Locate every blood parasite and identify its species.
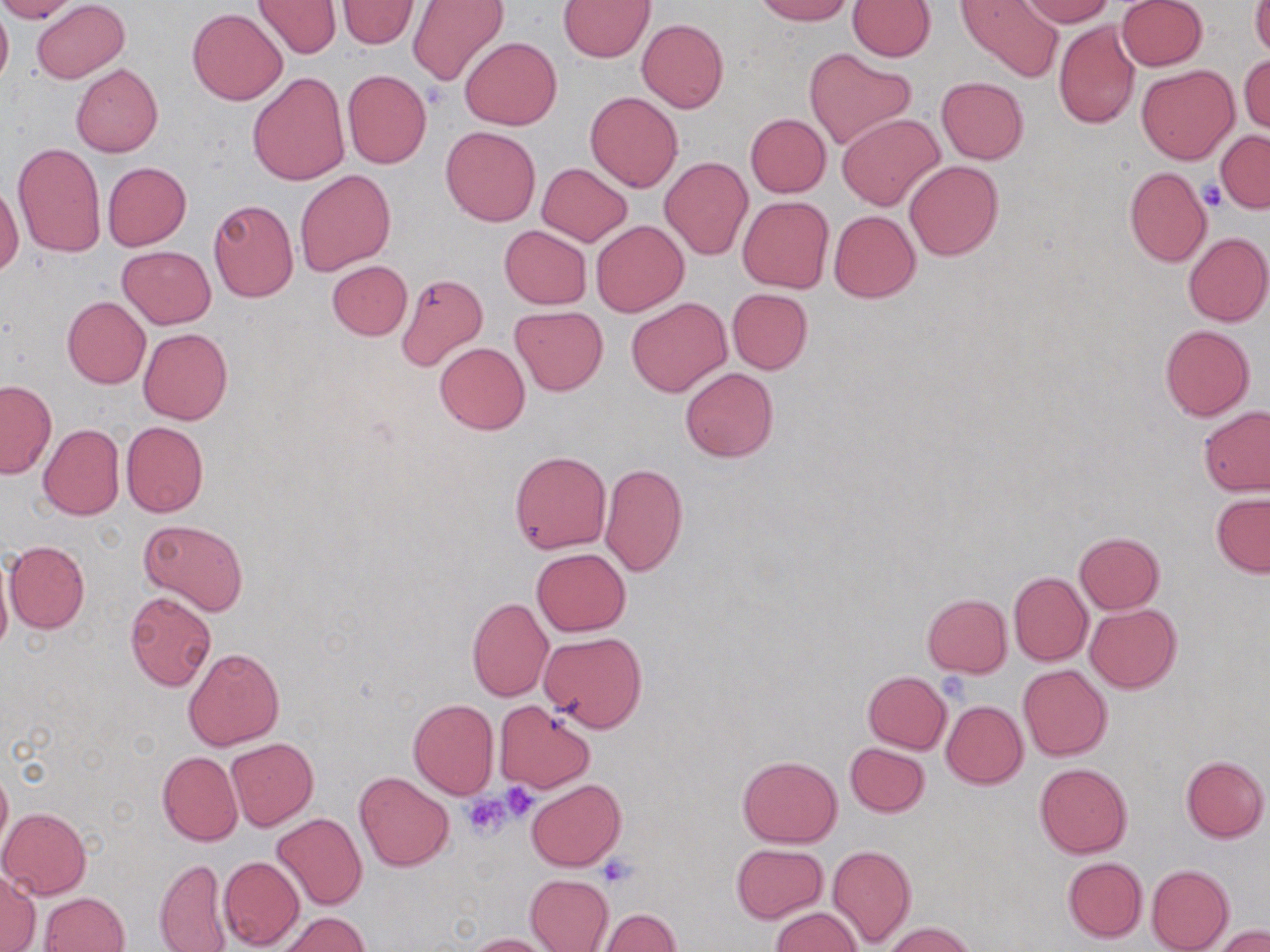

No blood parasites seen.

Approximate bounding boxes as [x1, y1, x2, y2] in pixels. Uninfected red blood cell locations: [0, 0, 12, 94], [0, 0, 79, 22], [32, 0, 130, 83], [254, 0, 342, 58], [753, 0, 854, 24], [956, 0, 1063, 80], [1020, 0, 1114, 26], [1116, 0, 1207, 71], [336, 1, 419, 49], [407, 1, 508, 86], [558, 1, 655, 61], [847, 1, 936, 60], [1250, 2, 1270, 58], [186, 8, 287, 105], [637, 18, 728, 112], [1052, 19, 1139, 129], [460, 37, 562, 130], [804, 48, 915, 150], [1240, 54, 1269, 134], [71, 64, 162, 157], [1136, 64, 1238, 164], [341, 69, 430, 169], [248, 72, 349, 185], [935, 76, 1029, 164], [585, 91, 683, 192], [745, 113, 831, 197], [837, 113, 944, 210], [441, 126, 541, 227], [1216, 129, 1269, 212], [13, 141, 105, 257], [659, 157, 753, 261], [905, 160, 1003, 260], [103, 162, 191, 250], [537, 163, 632, 245], [1123, 168, 1211, 267], [294, 169, 396, 276], [2, 184, 23, 272], [737, 195, 833, 293], [208, 199, 299, 302], [829, 210, 920, 302], [591, 221, 688, 316], [499, 226, 591, 309], [1183, 232, 1270, 326], [118, 245, 216, 329], [327, 260, 412, 340], [395, 273, 487, 371], [727, 288, 813, 374], [62, 296, 150, 389], [626, 298, 731, 397], [510, 306, 608, 395], [1160, 325, 1255, 421], [139, 328, 232, 424], [434, 341, 530, 435], [680, 367, 779, 462], [0, 380, 56, 478], [1199, 405, 1270, 496], [122, 421, 208, 517], [39, 424, 125, 521], [509, 451, 612, 554], [599, 464, 688, 576], [1211, 493, 1270, 577], [139, 519, 248, 616], [1074, 531, 1165, 614], [4, 541, 90, 633], [532, 548, 631, 637], [0, 558, 12, 661], [1009, 572, 1093, 665], [125, 592, 216, 691], [922, 593, 1012, 677], [466, 597, 554, 702], [1084, 602, 1181, 693], [539, 631, 648, 732], [181, 647, 284, 751], [1018, 664, 1112, 761], [863, 671, 952, 753], [407, 699, 498, 799], [495, 701, 595, 794], [941, 701, 1028, 788], [227, 738, 318, 830], [845, 743, 930, 817], [157, 751, 243, 845], [737, 755, 843, 847], [1180, 755, 1268, 842], [1, 760, 12, 857], [1035, 763, 1132, 858], [354, 771, 454, 871], [526, 778, 626, 871], [0, 807, 91, 899], [273, 812, 367, 910], [731, 843, 829, 924], [828, 844, 917, 948], [218, 855, 303, 950], [155, 857, 230, 952], [1062, 857, 1147, 942], [1147, 864, 1234, 952], [0, 871, 40, 951], [525, 874, 614, 951], [40, 892, 130, 952], [771, 907, 862, 952], [596, 908, 681, 952], [277, 911, 370, 951], [882, 922, 979, 952], [1214, 926, 1269, 952], [465, 933, 556, 952]. Platelet locations: [1200, 178, 1227, 210], [500, 783, 540, 820], [463, 794, 512, 840], [600, 858, 635, 887]. Slide-level diagnosis: no evidence of blood parasites. One field of a larger specimen. Image is 1270×952 pixels. Thin blood film. Light microscopy. 1000x magnification. May-Grünwald-Giemsa-stained preparation.